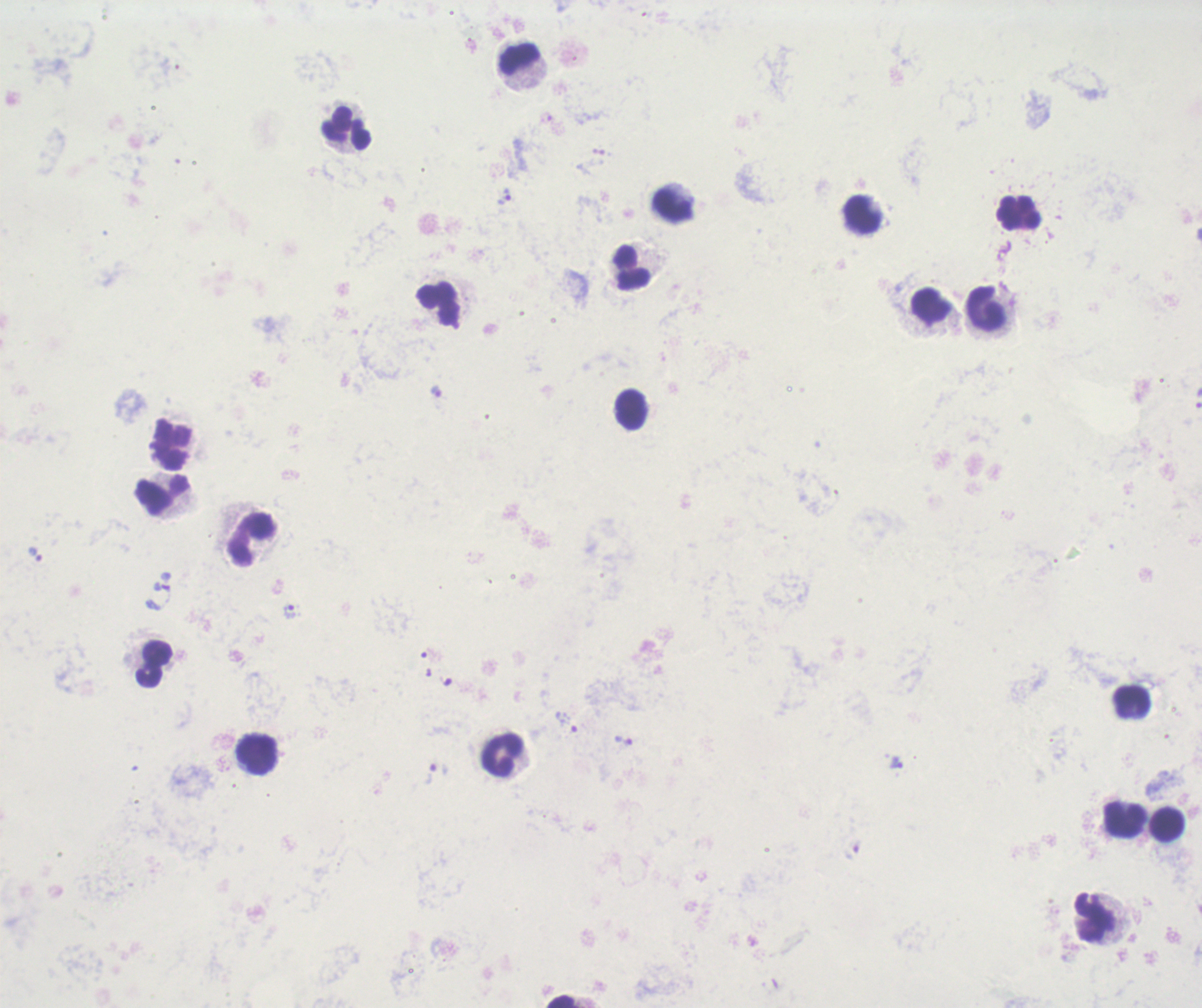

Approximate centers as (x, y) in pixels. Trophozoite locations: (505, 196), (435, 391), (36, 555), (158, 596), (290, 611), (566, 723), (896, 762), (431, 773). Leukocyte locations: (519, 59), (345, 129), (672, 204), (1019, 212), (862, 215), (632, 268), (438, 304), (931, 304), (986, 307), (631, 410), (171, 443), (162, 495), (252, 538), (158, 653), (149, 677), (1132, 701), (256, 754), (502, 755), (1125, 819), (1168, 824), (1095, 915), (565, 1001). Thick blood smear. Background quality: poor. Image is 1202×1008 pixels. Romanowsky-stained preparation. Result: positive for Plasmodium parasites. Previously used in a real diagnosis. 100x magnification. Single field of view.